Report the malaria status.
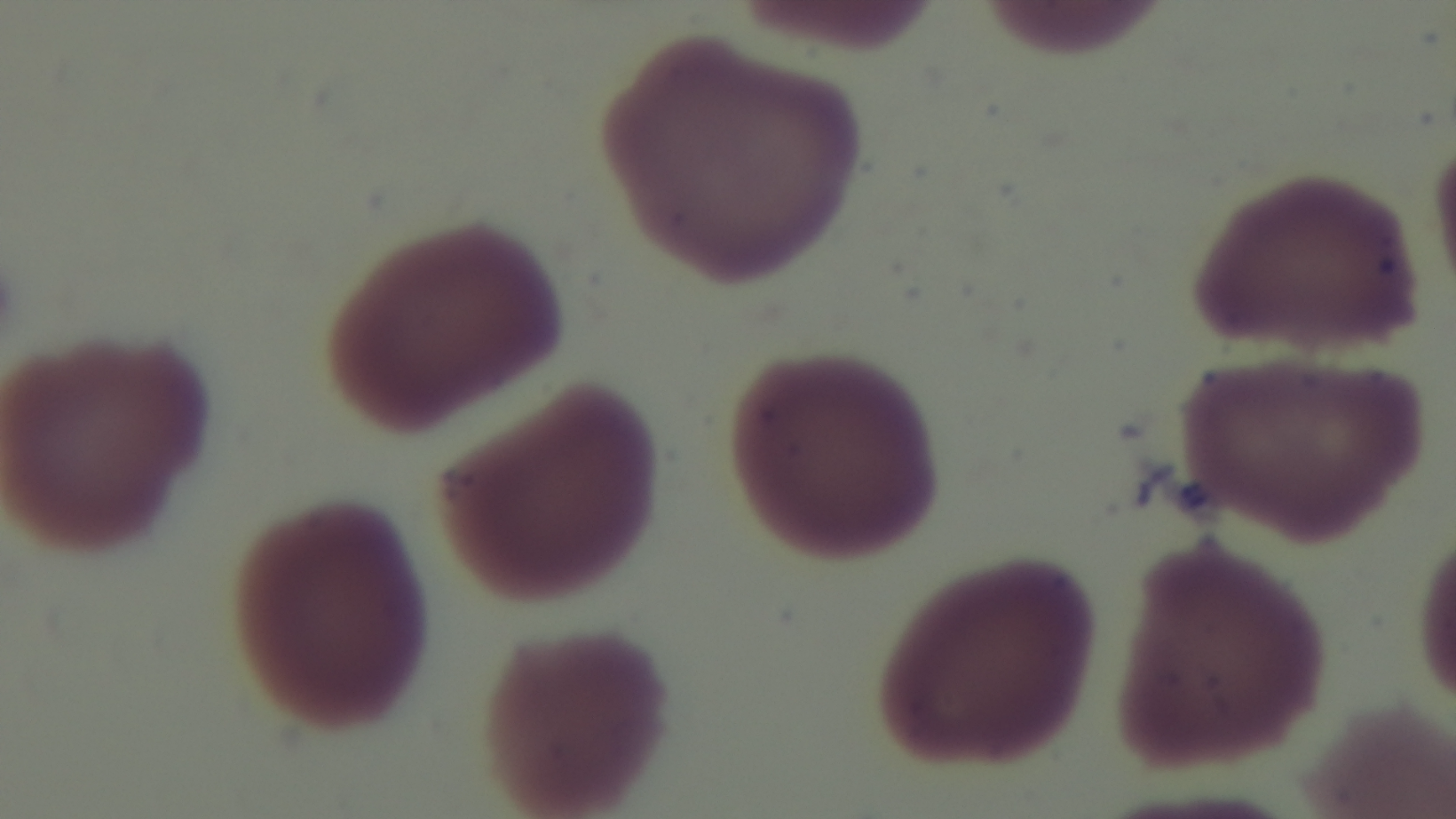

Negative.

Photomicrograph. Captured with a mounted 4K digital camera. Oil-immersion objective, 100x. Giemsa-stained. Preparation: thin. Single field of view.